Locate every white blood cell.
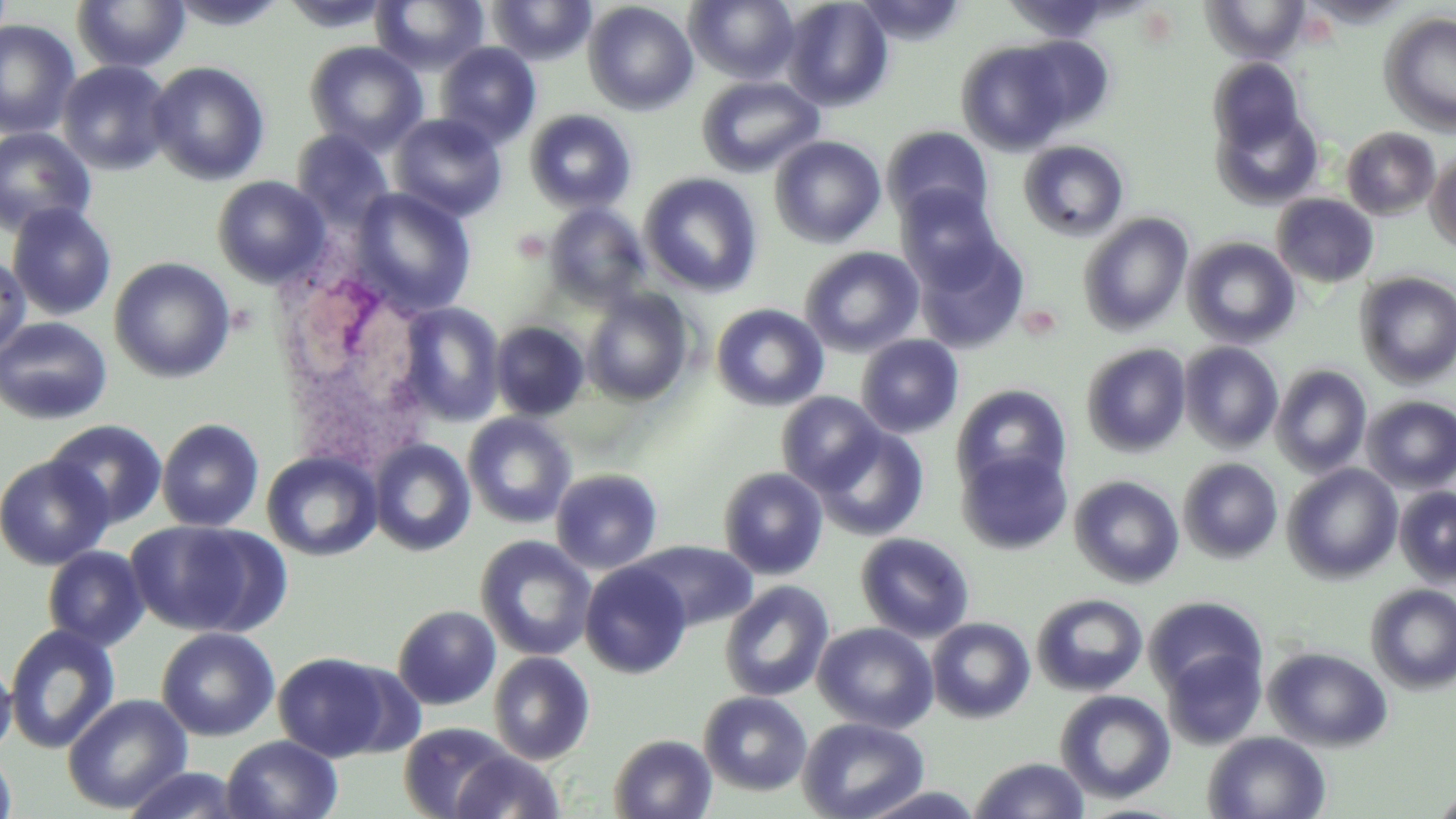
Approximate bounding boxes as (x1, y1, x2, y2) in pixels.
White blood cells: (271, 263, 434, 455).

Uninfected red blood cell locations: (370, 0, 489, 73), (488, 0, 596, 66), (686, 0, 799, 84), (782, 0, 894, 111), (855, 0, 967, 44), (1003, 0, 1116, 43), (1204, 0, 1309, 62), (72, 1, 191, 72), (583, 1, 698, 115), (1379, 12, 1456, 135), (0, 20, 80, 139), (1016, 36, 1115, 131), (304, 41, 428, 153), (435, 42, 541, 147), (956, 42, 1073, 155), (1209, 59, 1305, 151), (57, 60, 173, 175), (146, 61, 271, 185), (696, 75, 824, 178), (1212, 106, 1322, 210), (524, 109, 637, 214), (390, 113, 508, 221), (882, 125, 994, 224), (0, 127, 97, 237), (1341, 127, 1441, 220), (291, 129, 394, 228), (769, 135, 886, 248), (1018, 140, 1129, 241), (1426, 151, 1456, 253), (640, 173, 762, 297), (212, 176, 331, 287), (896, 184, 1002, 287), (351, 187, 476, 317), (1271, 193, 1379, 288), (6, 203, 118, 321), (544, 203, 649, 307), (1078, 213, 1193, 335), (913, 233, 1030, 354), (1183, 237, 1300, 349), (799, 246, 924, 357), (0, 253, 31, 360), (109, 257, 236, 383), (1356, 272, 1456, 387), (582, 288, 694, 406), (398, 302, 506, 426), (711, 303, 829, 411), (0, 316, 112, 425), (490, 320, 589, 421), (855, 334, 964, 438), (1178, 342, 1283, 452), (1080, 343, 1191, 457), (1270, 364, 1371, 476), (951, 384, 1071, 496), (776, 392, 885, 494), (1361, 396, 1456, 493), (462, 413, 577, 528), (156, 418, 265, 532), (45, 420, 169, 529), (810, 424, 929, 542), (369, 439, 475, 556), (956, 447, 1072, 555), (262, 451, 382, 561), (0, 454, 113, 570), (1178, 457, 1283, 564), (1282, 463, 1403, 582), (718, 467, 828, 579), (551, 468, 663, 575), (1069, 474, 1185, 589), (1394, 486, 1456, 587), (124, 520, 274, 637), (855, 532, 975, 642), (475, 535, 596, 661), (629, 540, 758, 631), (42, 546, 149, 652), (580, 562, 691, 678), (719, 580, 834, 702), (1365, 584, 1456, 694), (1031, 593, 1148, 696), (1143, 595, 1268, 700), (393, 605, 501, 710), (926, 617, 1035, 723), (813, 622, 938, 733), (4, 624, 121, 753), (156, 627, 281, 741), (1264, 646, 1394, 752), (1161, 648, 1266, 749), (274, 652, 396, 761), (489, 652, 595, 764), (0, 658, 17, 759), (1055, 689, 1176, 803), (699, 692, 812, 795), (61, 693, 193, 814), (798, 717, 929, 819), (399, 722, 517, 818), (1203, 731, 1332, 818), (608, 734, 717, 819), (222, 735, 343, 819), (0, 748, 17, 818), (448, 749, 566, 818), (969, 757, 1090, 818), (120, 767, 249, 818), (854, 786, 988, 818), (1431, 788, 1456, 818). Slide-level diagnosis: no evidence of blood parasites. Light microscopy. Thin blood smear. Image is 1456×819 pixels. May-Grünwald-Giemsa-stained preparation. 1000x magnification. Single field of view.